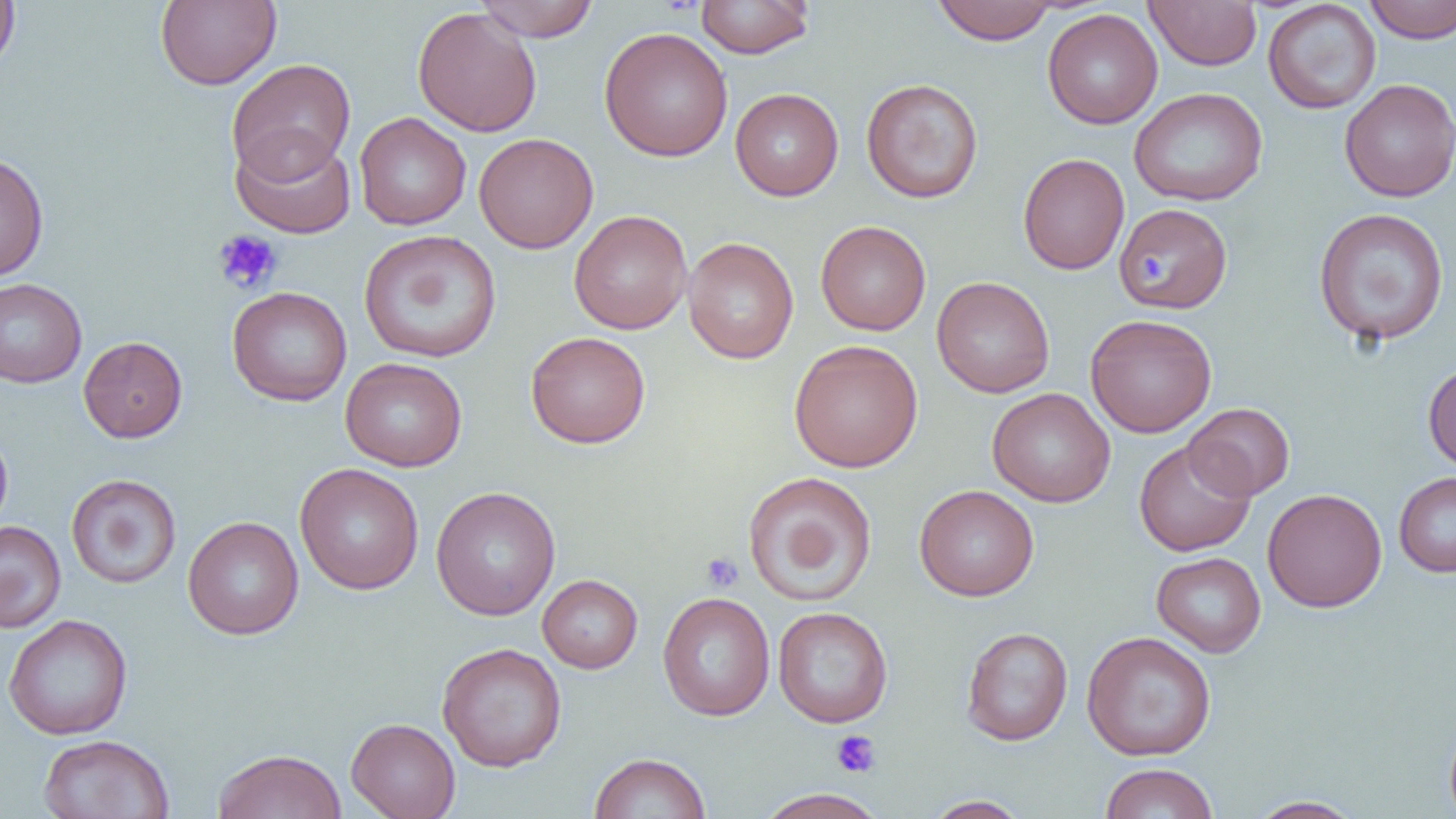

Approximate bounding boxes as (x1, y1, x2, y2) in pixels. Uninfected red blood cell locations: (0, 0, 20, 75), (155, 0, 282, 89), (473, 0, 600, 42), (695, 0, 815, 58), (1144, 0, 1263, 71), (1363, 0, 1456, 44), (930, 1, 1059, 44), (1263, 1, 1381, 115), (412, 7, 543, 137), (1042, 8, 1163, 129), (599, 26, 733, 162), (226, 58, 355, 183), (861, 78, 984, 203), (1339, 78, 1456, 202), (730, 87, 844, 201), (1128, 87, 1268, 206), (354, 112, 471, 230), (230, 132, 357, 240), (473, 133, 598, 253), (0, 152, 49, 281), (1017, 153, 1129, 275), (1116, 202, 1233, 313), (1313, 208, 1450, 345), (569, 210, 692, 334), (815, 220, 931, 335), (358, 230, 502, 363), (682, 236, 799, 364), (932, 276, 1055, 398), (0, 278, 87, 388), (226, 286, 352, 407), (1085, 313, 1217, 438), (525, 332, 651, 449), (78, 336, 188, 442), (789, 339, 923, 473), (340, 357, 468, 472), (1423, 362, 1456, 473), (987, 387, 1115, 507), (1184, 402, 1295, 500), (0, 425, 13, 535), (1133, 439, 1255, 556), (295, 463, 424, 595), (741, 471, 877, 607), (1394, 471, 1456, 578), (66, 473, 182, 589), (914, 484, 1039, 601), (430, 486, 561, 620), (1262, 488, 1387, 612), (183, 515, 304, 640), (0, 520, 66, 633), (1151, 551, 1266, 657), (537, 574, 643, 673), (658, 592, 775, 721), (772, 607, 893, 727), (3, 614, 133, 740), (960, 626, 1073, 745), (1081, 631, 1217, 760), (436, 642, 567, 771), (1444, 710, 1456, 819), (346, 717, 461, 819), (38, 734, 175, 819), (212, 748, 346, 819), (589, 752, 711, 819), (1099, 762, 1218, 819), (754, 788, 890, 819), (922, 796, 1031, 818), (1247, 796, 1364, 818). Platelet locations: (213, 229, 282, 294), (1138, 256, 1166, 287), (701, 552, 744, 593), (831, 731, 881, 778). Slide-level diagnosis: no evidence of blood parasites. Thin blood smear. Single field of view. 1000x magnification. Image is 1456×819 pixels. Light microscopy.